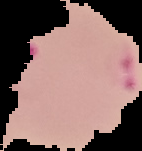

From a thin blood film. Image is 142×151 pixels. Result: malaria parasites detected. The area outside the segmented cell region is set to black.